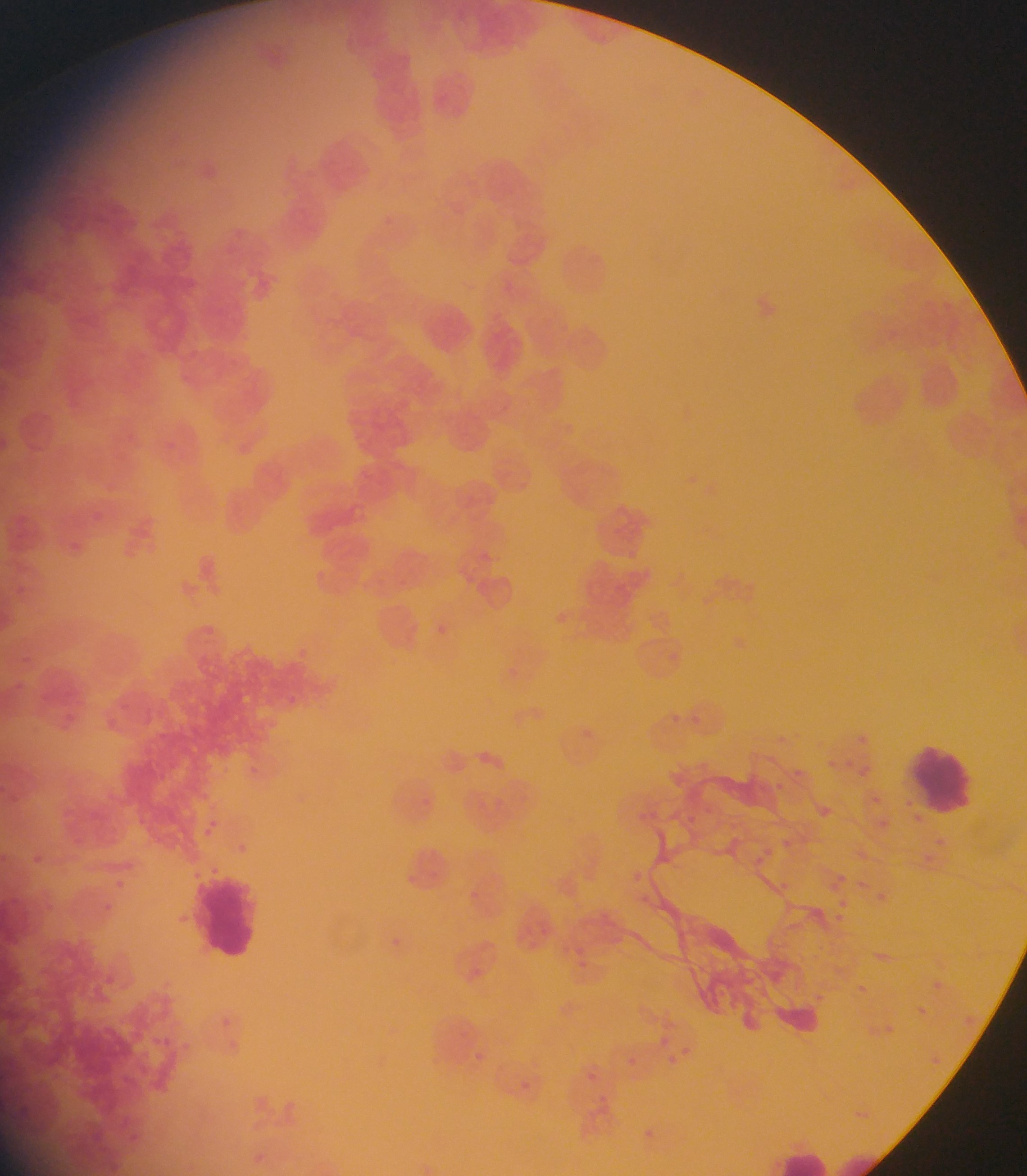

image_size: 1027×1176 pixels
preparation: thin blood film
leukocyte_locations: 'approximate bounding boxes as [left, top, right, bottom] in pixels: [908, 740, 969, 814], [191, 872, 268, 960], [763, 1133, 904, 1176]'
country: Ghana
field_of_view: single
capture: mobile-phone photograph through a microscope